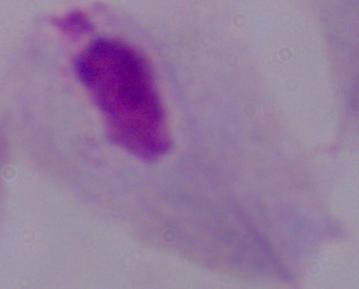

modality = micrograph
identification = trichomonad
magnification = 1000x